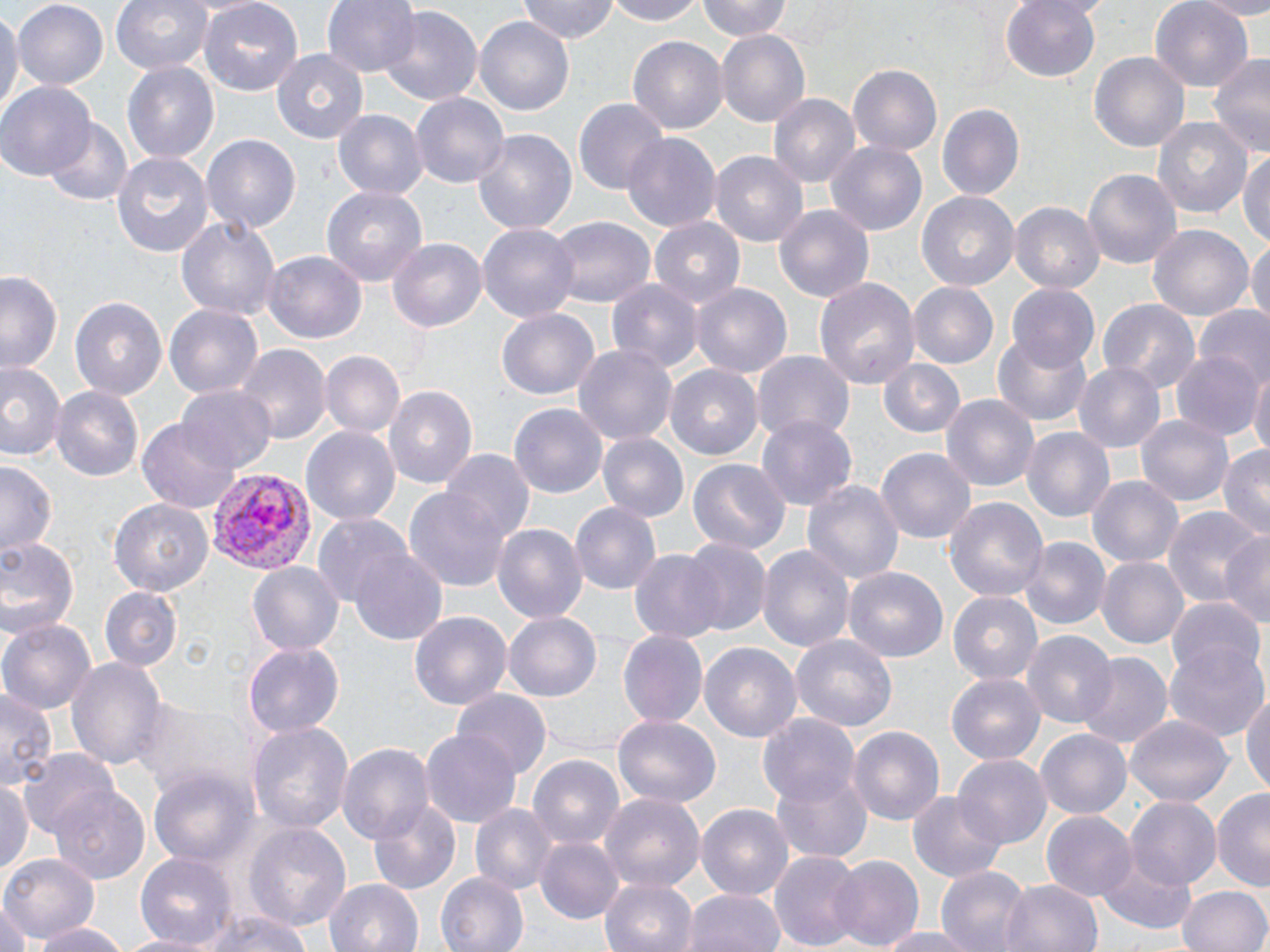
Summary:
  - Coordinate format: approximate bounding boxes as (x1, y1, x2, y2) in pixels
  - Plasmodium vivax-infected red blood cell locations: (206, 468, 315, 577)
  - Uninfected red blood cell locations: (109, 0, 216, 77), (196, 0, 304, 96), (322, 0, 421, 78), (516, 0, 620, 44), (602, 0, 710, 26), (696, 0, 794, 41), (999, 0, 1105, 84), (1192, 0, 1270, 18), (1151, 1, 1255, 92), (12, 2, 111, 89), (0, 4, 19, 119), (377, 5, 482, 107), (474, 18, 574, 113), (716, 29, 810, 126), (627, 36, 726, 134), (271, 47, 372, 143), (1089, 51, 1190, 154), (1206, 52, 1270, 160), (122, 61, 218, 164), (847, 63, 943, 155), (1, 82, 96, 180), (770, 94, 861, 189), (410, 95, 507, 187), (573, 96, 668, 195), (937, 103, 1025, 201), (332, 108, 428, 200), (1151, 116, 1254, 221), (44, 118, 133, 207), (471, 127, 579, 238), (622, 132, 721, 235), (200, 134, 302, 235), (827, 143, 928, 234), (1238, 148, 1270, 250), (111, 150, 215, 257), (710, 152, 810, 247), (1083, 168, 1181, 270), (321, 184, 428, 288), (917, 191, 1020, 291), (1010, 201, 1103, 292), (772, 202, 876, 305), (175, 215, 278, 323), (546, 216, 656, 307), (649, 217, 748, 309), (477, 223, 581, 324), (1147, 223, 1253, 322), (1249, 235, 1269, 332), (388, 236, 486, 332), (264, 252, 366, 343), (0, 269, 64, 372), (813, 276, 919, 390), (608, 281, 703, 375), (907, 282, 998, 370), (1008, 283, 1101, 372), (693, 284, 790, 378), (69, 297, 168, 400), (1098, 298, 1199, 396), (165, 303, 264, 398), (495, 306, 602, 400), (1195, 306, 1270, 390), (992, 332, 1092, 424), (574, 343, 677, 449), (236, 346, 328, 446), (1172, 350, 1262, 441), (318, 351, 404, 439), (752, 352, 854, 447), (0, 359, 65, 465), (881, 359, 966, 439), (1073, 361, 1163, 453), (665, 365, 763, 460), (1248, 367, 1270, 460), (386, 384, 477, 492), (52, 386, 144, 483), (178, 386, 277, 472), (939, 392, 1040, 490), (512, 404, 606, 500), (1136, 411, 1233, 506), (757, 416, 856, 512), (137, 419, 241, 513), (300, 424, 400, 525), (1023, 426, 1116, 523), (598, 431, 688, 521), (1217, 443, 1270, 542), (876, 448, 974, 548), (440, 452, 533, 545), (687, 456, 790, 554), (1, 459, 60, 558), (1087, 473, 1183, 567), (802, 477, 903, 589), (405, 490, 514, 592), (946, 495, 1048, 606), (108, 498, 213, 597), (570, 501, 660, 597), (1164, 507, 1266, 609), (312, 515, 412, 610), (492, 521, 588, 625), (1221, 530, 1270, 629), (0, 534, 82, 638), (1021, 538, 1109, 628), (678, 539, 769, 635), (758, 544, 853, 657), (349, 548, 448, 647), (629, 549, 726, 644), (1097, 556, 1188, 649), (247, 560, 343, 655), (846, 568, 946, 664), (99, 588, 180, 671), (948, 590, 1042, 686), (1165, 600, 1265, 685), (410, 610, 513, 711), (504, 611, 602, 702), (0, 619, 96, 712), (617, 630, 707, 727), (1023, 631, 1117, 731), (790, 634, 898, 731), (1164, 640, 1269, 743), (243, 642, 344, 737), (700, 642, 801, 742), (1077, 652, 1171, 749), (66, 657, 166, 770), (946, 673, 1045, 765), (1242, 683, 1270, 802), (454, 689, 554, 778), (0, 690, 57, 792), (130, 695, 249, 798), (611, 713, 718, 808), (757, 714, 861, 808), (1126, 714, 1232, 807), (247, 720, 352, 834), (420, 723, 519, 827), (848, 726, 944, 827), (1037, 729, 1132, 820), (337, 742, 434, 844), (18, 749, 122, 844), (528, 753, 624, 851), (953, 755, 1049, 850), (150, 767, 257, 870), (772, 767, 874, 862), (0, 781, 32, 880), (50, 787, 150, 884), (1211, 788, 1270, 893), (909, 791, 1007, 883), (602, 793, 703, 890), (1127, 797, 1220, 889), (370, 801, 460, 893), (696, 802, 794, 901), (470, 803, 556, 896), (1041, 811, 1137, 903), (243, 820, 352, 935), (534, 836, 624, 925), (770, 849, 865, 952), (134, 850, 236, 946), (1096, 850, 1199, 935), (1, 853, 99, 944), (827, 854, 925, 950), (935, 866, 1031, 952), (437, 872, 527, 951), (600, 876, 700, 952), (325, 877, 424, 952), (1001, 877, 1102, 952), (1178, 884, 1269, 952), (686, 889, 786, 952), (0, 901, 30, 952), (189, 910, 315, 952), (30, 921, 130, 952), (871, 926, 983, 951), (114, 932, 215, 952)
  - Slide-level diagnosis: Plasmodium vivax
  - Image size: 1270×952 pixels
  - Modality: light microscopy
  - Field of view: single
  - Magnification: 1000x
  - Preparation: thin blood film
  - Stain: May-Grünwald-Giemsa